Assess this cell for malaria.
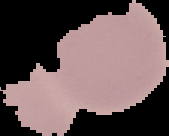

It is uninfected.

image size = 169×136 pixels
preparation = thin blood smear
image type = segmented cell region with the area outside set to black